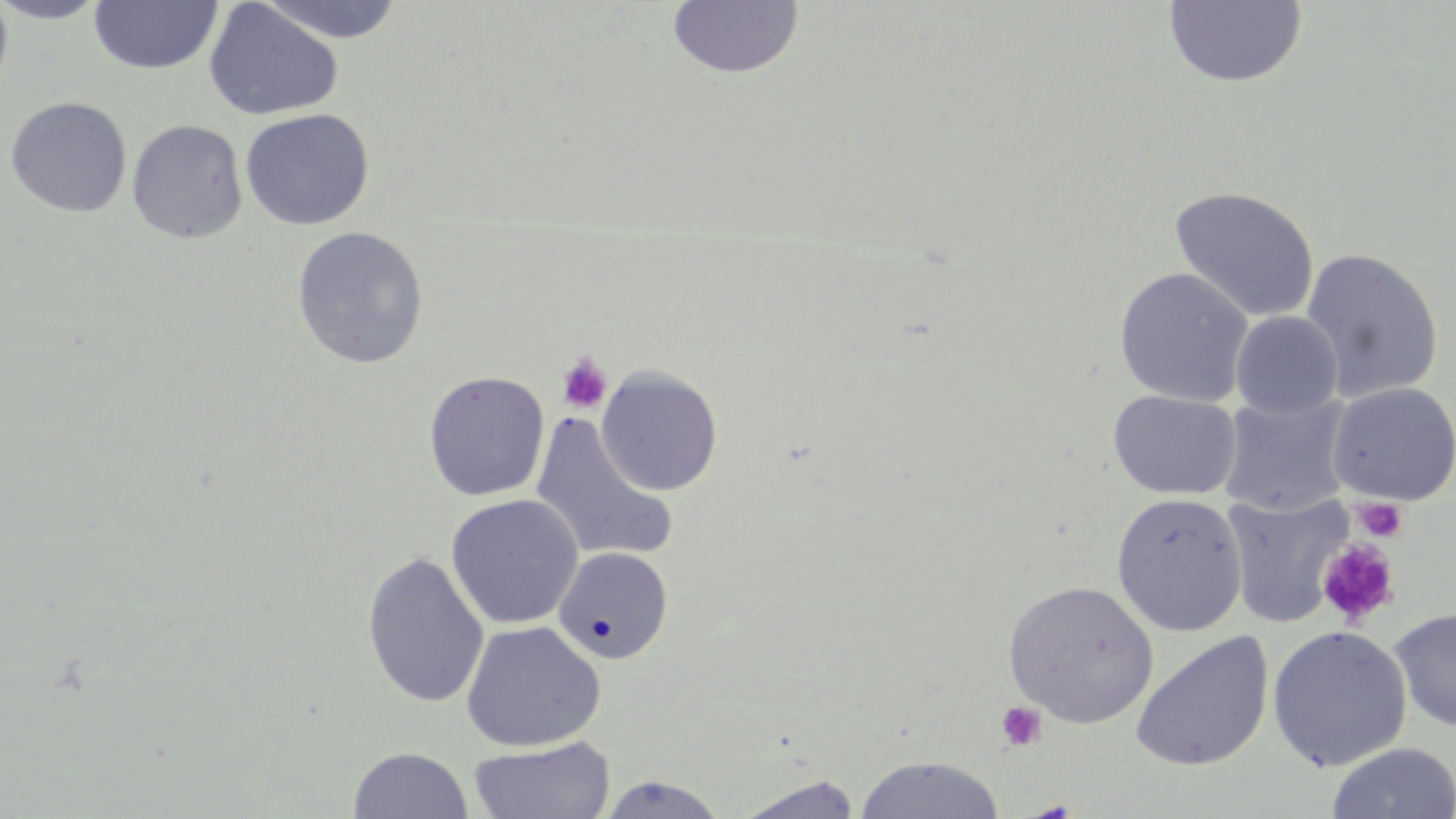
Summary:
  - Coordinate format: approximate bounding boxes as (x1,y1)-(x2,y2) corner pairs in pixels
  - Uninfected red blood cell locations: (0,0)-(14,100), (0,0)-(110,24), (89,0)-(222,76), (256,0)-(406,44), (203,1)-(343,121), (1163,1)-(1309,88), (666,2)-(804,81), (4,97)-(132,218), (239,108)-(375,230), (127,119)-(248,245), (1169,186)-(1320,323), (292,226)-(429,369), (1299,247)-(1444,403), (1113,266)-(1254,408), (1230,311)-(1343,420), (595,367)-(723,496), (423,371)-(549,502), (1326,382)-(1456,505), (1108,389)-(1241,500), (1219,393)-(1352,516), (530,414)-(678,565), (1111,492)-(1248,636), (1223,492)-(1352,628), (445,493)-(584,629), (552,546)-(673,664), (361,550)-(490,709), (1003,580)-(1158,728), (1389,606)-(1456,732), (460,621)-(606,752), (1267,625)-(1413,771), (1130,631)-(1273,772), (467,737)-(616,819), (1325,743)-(1456,819), (348,746)-(473,819), (854,755)-(1007,818), (595,773)-(729,818), (732,775)-(865,819)
  - Platelet locations: (556,352)-(613,414), (1354,496)-(1407,543), (1316,537)-(1399,627), (995,701)-(1048,752)
  - Slide-level diagnosis: no evidence of blood parasites
  - Modality: optical microscopy
  - Magnification: 1000x
  - Preparation: thin blood film
  - Stain: May-Grünwald-Giemsa
  - Field of view: single
  - Image size: 1456×819 pixels